Assess the morphology of the erythrocytes.
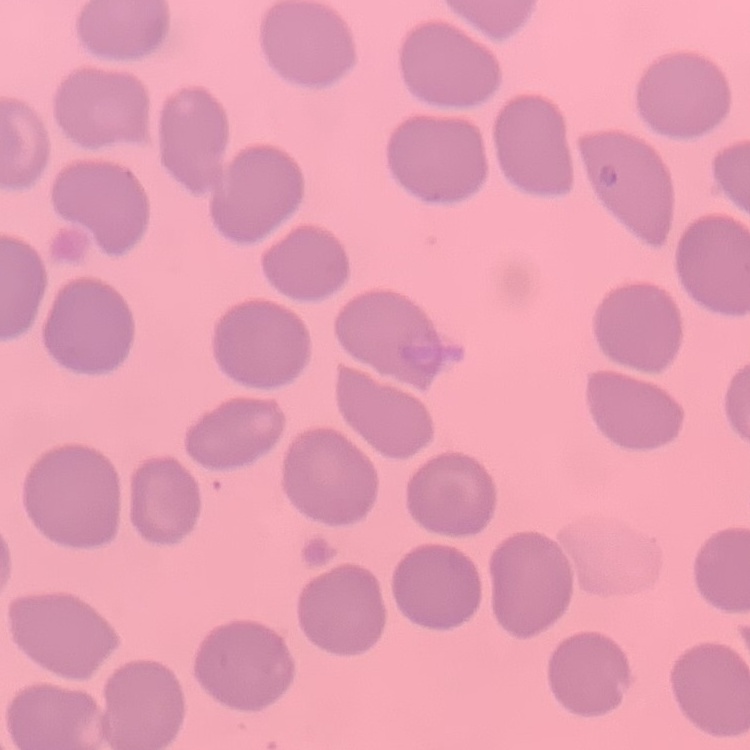
They show no rouleaux formation.

Summary:
  - Image type: one tile cut from a larger photomicrograph
  - Preparation: thin blood film
  - Stain: Field's or Giemsa